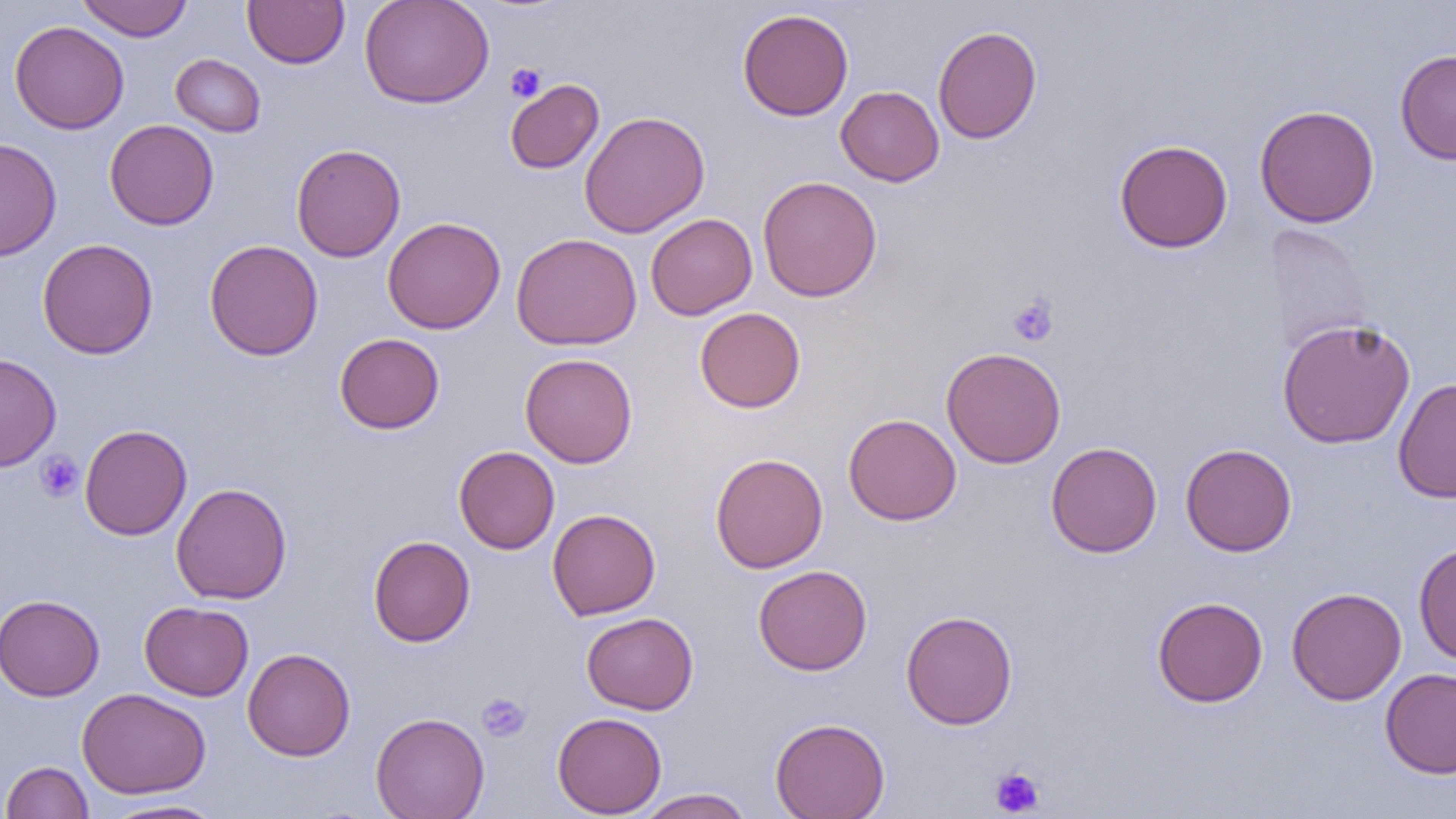
{
  "slide_level_diagnosis": "negative for blood parasites",
  "image_size": "1456×819 pixels",
  "field_of_view": "single",
  "platelet_locations": "approximate bounding boxes as [x1, y1, x2, y2] in pixels: [505, 63, 546, 103], [1008, 295, 1059, 346], [35, 452, 83, 502], [477, 693, 531, 742], [990, 766, 1045, 817]",
  "preparation": "thin blood smear",
  "magnification": "1000x",
  "modality": "light microscopy",
  "uninfected_red_blood_cell_locations": "approximate bounding boxes as [x1, y1, x2, y2] in pixels: [76, 0, 193, 41], [242, 0, 350, 68], [359, 0, 494, 109], [737, 8, 854, 121], [9, 20, 129, 135], [932, 25, 1042, 144], [1395, 49, 1456, 165], [170, 53, 266, 137], [505, 79, 604, 174], [836, 86, 945, 186], [1254, 104, 1380, 228], [579, 111, 710, 238], [104, 119, 219, 230], [0, 137, 62, 262], [1114, 139, 1233, 253], [291, 143, 406, 262], [757, 175, 883, 303], [645, 213, 757, 320], [382, 216, 506, 334], [1261, 224, 1371, 353], [511, 232, 642, 351], [37, 238, 159, 360], [204, 239, 323, 361], [694, 307, 806, 413], [1276, 317, 1416, 449], [334, 333, 445, 434], [940, 347, 1067, 469], [520, 352, 638, 468], [0, 353, 61, 472], [1393, 378, 1456, 503], [843, 413, 962, 525], [79, 423, 192, 540], [1046, 442, 1162, 557], [1180, 443, 1297, 556], [454, 446, 560, 554], [710, 452, 828, 573], [171, 483, 292, 605], [547, 508, 661, 620], [368, 535, 475, 647], [1413, 541, 1456, 666], [752, 565, 872, 675], [1286, 587, 1407, 705], [0, 594, 105, 701], [1152, 596, 1268, 707], [139, 601, 253, 701], [900, 610, 1018, 729], [581, 612, 698, 715], [242, 648, 356, 761], [1379, 667, 1456, 779], [77, 688, 211, 799], [370, 711, 490, 819], [552, 712, 666, 817], [770, 716, 890, 819], [1, 761, 93, 818], [636, 788, 754, 818], [103, 798, 225, 819]"
}